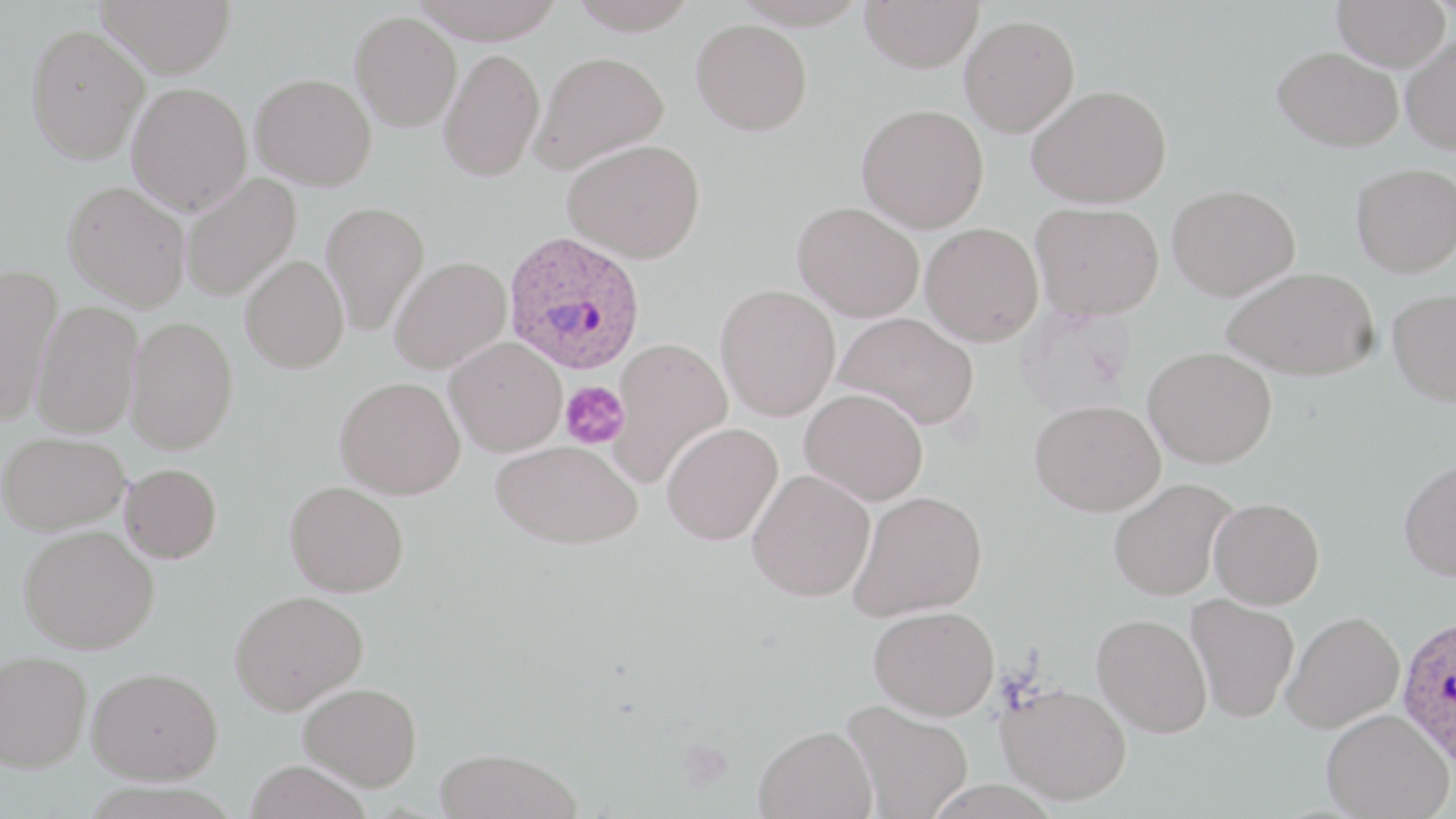

{
  "slide_level_diagnosis": "Plasmodium ovale",
  "stain": "May-Grünwald-Giemsa",
  "image_size": "1456×819 pixels",
  "plasmodium_ovale_infected_red_blood_cell_locations": "approximate bounding boxes as named x1/y1/x2/y2 corners in pixels: (x1=502, y1=233, x2=645, y2=378), (x1=1396, y1=612, x2=1456, y2=771)",
  "preparation": "thin blood film",
  "magnification": "1000x",
  "modality": "optical microscopy",
  "field_of_view": "one of a larger specimen",
  "platelet_locations": "approximate bounding boxes as named x1/y1/x2/y2 corners in pixels: (x1=561, y1=381, x2=630, y2=449)",
  "uninfected_red_blood_cell_locations": "approximate bounding boxes as named x1/y1/x2/y2 corners in pixels: (x1=97, y1=0, x2=235, y2=78), (x1=409, y1=0, x2=565, y2=43), (x1=568, y1=0, x2=700, y2=35), (x1=860, y1=0, x2=983, y2=73), (x1=1332, y1=0, x2=1450, y2=71), (x1=350, y1=12, x2=462, y2=132), (x1=959, y1=14, x2=1080, y2=137), (x1=692, y1=19, x2=812, y2=136), (x1=25, y1=23, x2=149, y2=165), (x1=1401, y1=34, x2=1456, y2=154), (x1=1273, y1=46, x2=1403, y2=152), (x1=439, y1=48, x2=544, y2=182), (x1=530, y1=51, x2=670, y2=174), (x1=250, y1=72, x2=377, y2=191), (x1=126, y1=81, x2=252, y2=217), (x1=1026, y1=84, x2=1171, y2=208), (x1=857, y1=103, x2=989, y2=233), (x1=562, y1=138, x2=706, y2=263), (x1=1351, y1=163, x2=1456, y2=277), (x1=180, y1=172, x2=301, y2=301), (x1=63, y1=180, x2=191, y2=312), (x1=1167, y1=184, x2=1299, y2=301), (x1=320, y1=200, x2=430, y2=336), (x1=794, y1=201, x2=925, y2=322), (x1=1032, y1=202, x2=1164, y2=318), (x1=920, y1=222, x2=1044, y2=346), (x1=240, y1=254, x2=349, y2=373), (x1=389, y1=257, x2=511, y2=374), (x1=0, y1=263, x2=63, y2=424), (x1=1221, y1=267, x2=1379, y2=381), (x1=715, y1=283, x2=841, y2=421), (x1=1387, y1=287, x2=1456, y2=406), (x1=31, y1=300, x2=143, y2=437), (x1=834, y1=311, x2=979, y2=429), (x1=125, y1=316, x2=239, y2=454), (x1=445, y1=337, x2=567, y2=457), (x1=609, y1=337, x2=732, y2=486), (x1=1144, y1=346, x2=1277, y2=468), (x1=335, y1=376, x2=465, y2=499), (x1=800, y1=387, x2=929, y2=505), (x1=1029, y1=399, x2=1165, y2=516), (x1=662, y1=422, x2=782, y2=545), (x1=1, y1=431, x2=130, y2=535), (x1=491, y1=440, x2=642, y2=549), (x1=1398, y1=458, x2=1456, y2=581), (x1=120, y1=463, x2=222, y2=563), (x1=747, y1=468, x2=876, y2=601), (x1=1108, y1=477, x2=1237, y2=601), (x1=284, y1=480, x2=409, y2=597), (x1=849, y1=490, x2=987, y2=621), (x1=1209, y1=497, x2=1324, y2=609), (x1=19, y1=525, x2=159, y2=654), (x1=229, y1=589, x2=368, y2=714), (x1=1185, y1=593, x2=1300, y2=723), (x1=869, y1=605, x2=1000, y2=719), (x1=1282, y1=611, x2=1404, y2=733), (x1=1092, y1=613, x2=1212, y2=737), (x1=0, y1=651, x2=92, y2=772), (x1=87, y1=666, x2=222, y2=784), (x1=298, y1=682, x2=422, y2=790), (x1=996, y1=682, x2=1131, y2=805), (x1=841, y1=700, x2=975, y2=819), (x1=1321, y1=708, x2=1453, y2=819), (x1=753, y1=725, x2=877, y2=819), (x1=434, y1=747, x2=585, y2=819), (x1=243, y1=759, x2=370, y2=819)"
}